Classify this cell by malaria status.
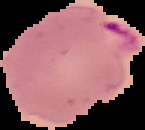
It is parasitized.

image size = 145×130 pixels
preparation = thin blood smear
image type = cell region segmented out of the field of view; surrounding area masked to black